Locate every uninfected red blood cell.
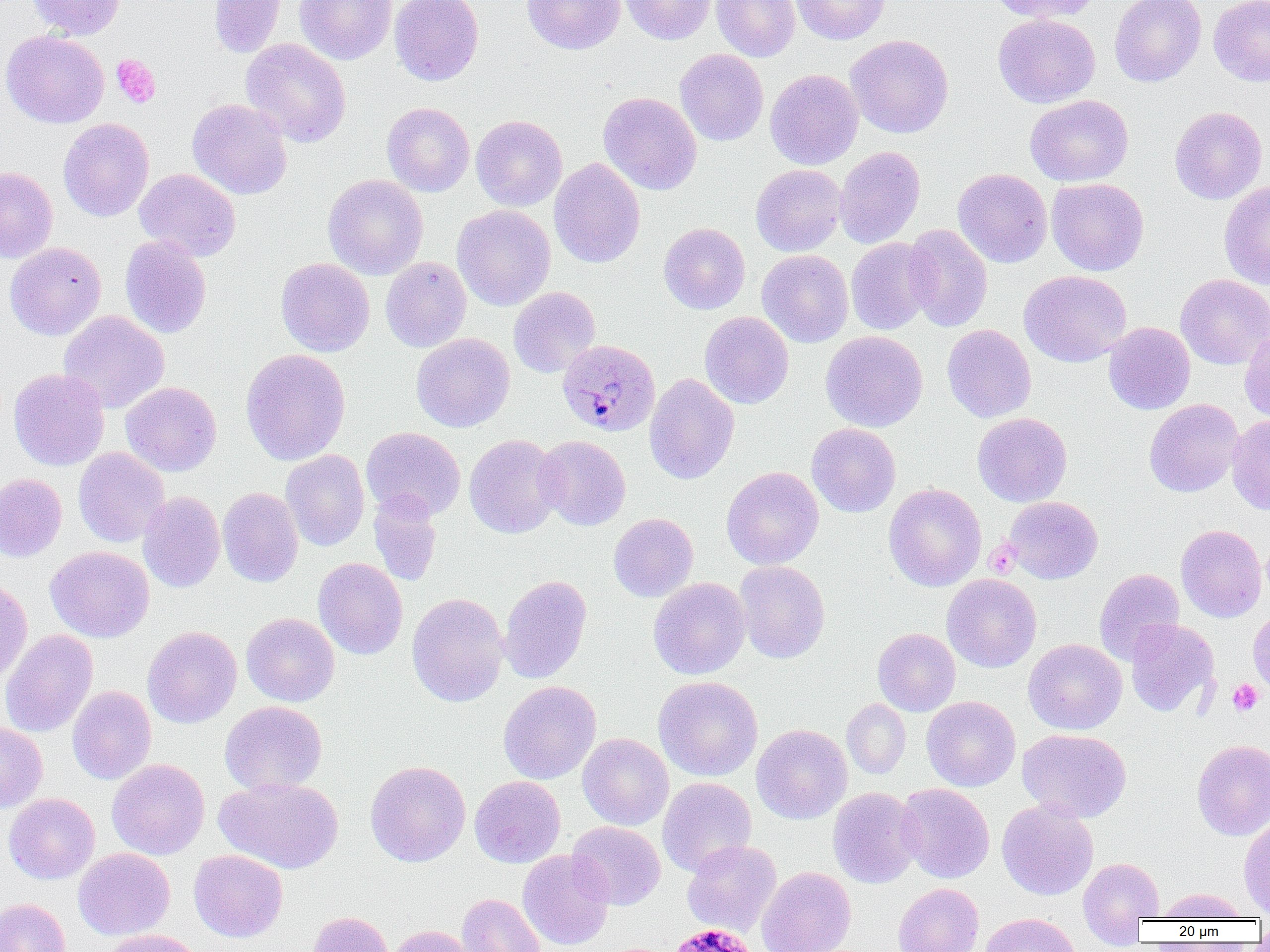

Approximate bounding boxes as named x1/y1/x2/y2 corners in pixels.
Uninfected red blood cells: (x1=27, y1=0, x2=126, y2=39), (x1=208, y1=0, x2=286, y2=58), (x1=295, y1=0, x2=397, y2=64), (x1=389, y1=0, x2=484, y2=86), (x1=522, y1=0, x2=626, y2=54), (x1=620, y1=0, x2=715, y2=45), (x1=712, y1=0, x2=800, y2=62), (x1=791, y1=0, x2=890, y2=44), (x1=988, y1=0, x2=1100, y2=23), (x1=1109, y1=0, x2=1206, y2=87), (x1=1208, y1=0, x2=1270, y2=86), (x1=993, y1=13, x2=1100, y2=108), (x1=1, y1=30, x2=109, y2=128), (x1=845, y1=34, x2=954, y2=139), (x1=241, y1=38, x2=351, y2=147), (x1=674, y1=49, x2=769, y2=146), (x1=765, y1=68, x2=864, y2=170), (x1=598, y1=92, x2=701, y2=195), (x1=1025, y1=95, x2=1133, y2=186), (x1=187, y1=98, x2=293, y2=199), (x1=382, y1=102, x2=474, y2=197), (x1=1169, y1=106, x2=1268, y2=204), (x1=471, y1=115, x2=567, y2=211), (x1=58, y1=118, x2=154, y2=221), (x1=835, y1=146, x2=925, y2=249), (x1=548, y1=158, x2=645, y2=268), (x1=751, y1=164, x2=847, y2=256), (x1=0, y1=166, x2=58, y2=263), (x1=135, y1=168, x2=241, y2=261), (x1=953, y1=168, x2=1052, y2=268), (x1=323, y1=174, x2=428, y2=280), (x1=1046, y1=177, x2=1149, y2=276), (x1=1219, y1=181, x2=1270, y2=290), (x1=452, y1=205, x2=555, y2=311), (x1=658, y1=223, x2=750, y2=314), (x1=902, y1=224, x2=992, y2=331), (x1=120, y1=235, x2=211, y2=338), (x1=845, y1=238, x2=938, y2=335), (x1=5, y1=242, x2=106, y2=340), (x1=757, y1=249, x2=853, y2=347), (x1=276, y1=257, x2=374, y2=356), (x1=380, y1=257, x2=471, y2=352), (x1=1019, y1=270, x2=1132, y2=367), (x1=1175, y1=274, x2=1270, y2=369), (x1=508, y1=287, x2=600, y2=377), (x1=59, y1=310, x2=169, y2=414), (x1=699, y1=311, x2=794, y2=409), (x1=1103, y1=321, x2=1195, y2=414), (x1=942, y1=324, x2=1036, y2=422), (x1=1240, y1=326, x2=1270, y2=424), (x1=820, y1=330, x2=928, y2=432), (x1=411, y1=333, x2=514, y2=432), (x1=240, y1=348, x2=351, y2=465), (x1=9, y1=368, x2=109, y2=471), (x1=644, y1=373, x2=739, y2=484), (x1=121, y1=382, x2=221, y2=476), (x1=1144, y1=399, x2=1243, y2=497), (x1=972, y1=413, x2=1072, y2=507), (x1=1227, y1=414, x2=1270, y2=515), (x1=807, y1=423, x2=901, y2=517), (x1=361, y1=427, x2=465, y2=521), (x1=464, y1=434, x2=563, y2=538), (x1=535, y1=435, x2=631, y2=531), (x1=74, y1=447, x2=170, y2=547), (x1=281, y1=450, x2=370, y2=551), (x1=722, y1=466, x2=824, y2=569), (x1=0, y1=473, x2=67, y2=562), (x1=884, y1=483, x2=986, y2=591), (x1=218, y1=487, x2=303, y2=587), (x1=138, y1=491, x2=225, y2=593), (x1=367, y1=491, x2=442, y2=586), (x1=1003, y1=496, x2=1103, y2=584), (x1=608, y1=513, x2=698, y2=602), (x1=1176, y1=524, x2=1266, y2=622), (x1=45, y1=546, x2=154, y2=642), (x1=313, y1=557, x2=407, y2=660), (x1=734, y1=560, x2=830, y2=663), (x1=1094, y1=568, x2=1184, y2=664), (x1=942, y1=574, x2=1041, y2=672), (x1=498, y1=575, x2=592, y2=684), (x1=0, y1=577, x2=32, y2=685), (x1=648, y1=577, x2=750, y2=679), (x1=407, y1=592, x2=509, y2=707), (x1=1248, y1=608, x2=1270, y2=699), (x1=241, y1=613, x2=340, y2=706), (x1=1125, y1=619, x2=1219, y2=717), (x1=142, y1=626, x2=242, y2=728), (x1=873, y1=628, x2=961, y2=716), (x1=0, y1=629, x2=98, y2=738), (x1=1023, y1=638, x2=1127, y2=735), (x1=653, y1=676, x2=763, y2=781), (x1=498, y1=681, x2=601, y2=784), (x1=67, y1=686, x2=157, y2=785), (x1=921, y1=696, x2=1021, y2=791), (x1=842, y1=698, x2=911, y2=779), (x1=220, y1=701, x2=327, y2=794), (x1=0, y1=722, x2=48, y2=813), (x1=751, y1=724, x2=852, y2=824), (x1=1018, y1=728, x2=1131, y2=822), (x1=577, y1=733, x2=674, y2=830), (x1=1192, y1=739, x2=1270, y2=840), (x1=107, y1=759, x2=210, y2=859), (x1=365, y1=760, x2=471, y2=867), (x1=470, y1=775, x2=566, y2=867), (x1=215, y1=776, x2=343, y2=873), (x1=657, y1=777, x2=756, y2=877), (x1=896, y1=783, x2=995, y2=883), (x1=827, y1=787, x2=923, y2=888), (x1=4, y1=793, x2=100, y2=884), (x1=997, y1=801, x2=1098, y2=900), (x1=1239, y1=819, x2=1270, y2=917), (x1=568, y1=821, x2=666, y2=910), (x1=682, y1=840, x2=782, y2=936), (x1=73, y1=848, x2=175, y2=940), (x1=188, y1=849, x2=288, y2=943), (x1=518, y1=849, x2=614, y2=950), (x1=1077, y1=856, x2=1163, y2=942), (x1=757, y1=866, x2=856, y2=952), (x1=893, y1=883, x2=984, y2=952), (x1=1157, y1=888, x2=1248, y2=921), (x1=456, y1=893, x2=545, y2=952), (x1=0, y1=898, x2=71, y2=952), (x1=305, y1=911, x2=393, y2=952), (x1=979, y1=912, x2=1081, y2=952), (x1=1252, y1=924, x2=1270, y2=948), (x1=388, y1=925, x2=476, y2=952), (x1=101, y1=929, x2=206, y2=952).

Plasmodium malariae-infected red blood cell locations: (x1=558, y1=339, x2=660, y2=436), (x1=667, y1=922, x2=761, y2=952). Platelet locations: (x1=111, y1=54, x2=160, y2=108), (x1=984, y1=540, x2=1021, y2=578), (x1=1227, y1=679, x2=1263, y2=716). Slide-level diagnosis: Plasmodium malariae. Image is 1270×952 pixels. Thin blood film. Light microscopy. 1000x magnification. One field of a larger specimen.